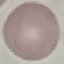

malaria status = uninfected
image type = cell patch, automatically extracted from a larger field of view and resized to 64 × 64 pixels
stain = Giemsa
capture = smartphone through the microscope eyepiece
preparation = thin blood smear